Assess this cell for malaria.
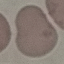

It is uninfected.

Summary:
  - Preparation: thin blood film
  - Capture: smartphone camera at the microscope eyepiece
  - Stain: Giemsa
  - Image type: automatically extracted cell patch, resized to 64 × 64 pixels